Classify this cell by malaria status.
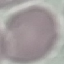
Uninfected.

Thin blood smear. Photographed with a smartphone camera at the microscope eyepiece. Automatically extracted cell patch, resized to 64 × 64 pixels. Giemsa-stained preparation.